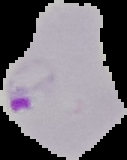

Result: Plasmodium parasites identified. Cell region segmented out of the field of view; the surrounding area is masked to black. From a thin blood smear. Image is 127×160 pixels.